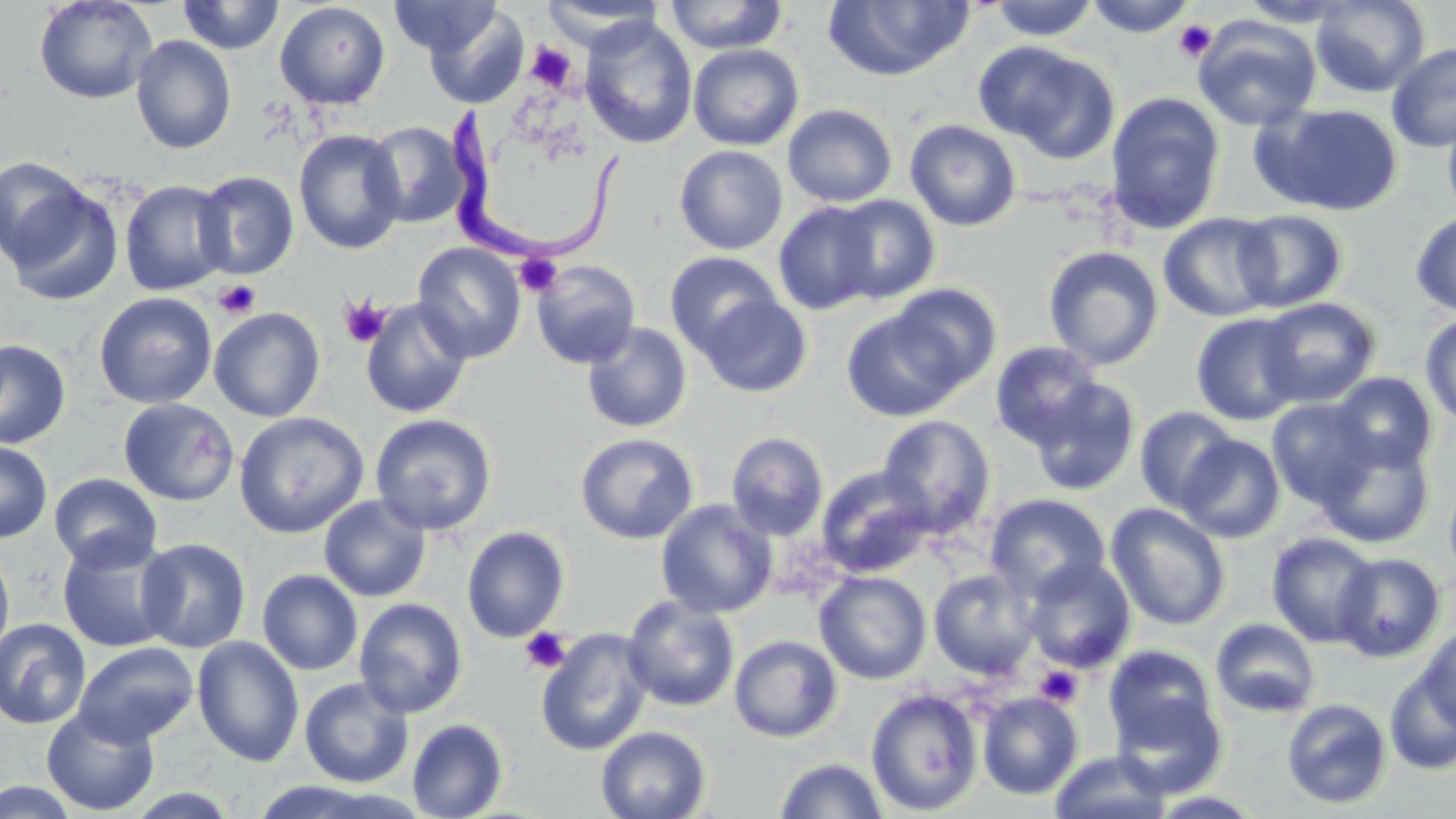

Summary:
  - Coordinate format: approximate bounding boxes as named x1/y1/x2/y2 corners in pixels
  - Uninfected red blood cell locations: (x1=34, y1=0, x2=158, y2=105), (x1=177, y1=0, x2=285, y2=55), (x1=391, y1=0, x2=498, y2=58), (x1=1084, y1=0, x2=1198, y2=38), (x1=1236, y1=0, x2=1357, y2=27), (x1=1310, y1=0, x2=1430, y2=97), (x1=539, y1=1, x2=666, y2=51), (x1=663, y1=1, x2=789, y2=54), (x1=821, y1=1, x2=975, y2=82), (x1=988, y1=1, x2=1099, y2=41), (x1=274, y1=2, x2=391, y2=110), (x1=424, y1=4, x2=528, y2=109), (x1=1192, y1=16, x2=1321, y2=131), (x1=579, y1=17, x2=698, y2=150), (x1=130, y1=35, x2=237, y2=154), (x1=977, y1=42, x2=1119, y2=160), (x1=1386, y1=42, x2=1456, y2=152), (x1=687, y1=43, x2=804, y2=150), (x1=1105, y1=92, x2=1226, y2=235), (x1=783, y1=103, x2=898, y2=208), (x1=1256, y1=103, x2=1404, y2=217), (x1=1441, y1=104, x2=1456, y2=224), (x1=905, y1=119, x2=1022, y2=232), (x1=365, y1=121, x2=468, y2=228), (x1=294, y1=129, x2=406, y2=255), (x1=674, y1=145, x2=788, y2=255), (x1=0, y1=155, x2=93, y2=270), (x1=193, y1=170, x2=299, y2=279), (x1=119, y1=179, x2=233, y2=296), (x1=3, y1=182, x2=124, y2=307), (x1=112, y1=182, x2=223, y2=409), (x1=827, y1=194, x2=941, y2=304), (x1=773, y1=201, x2=883, y2=315), (x1=1233, y1=210, x2=1348, y2=311), (x1=1410, y1=211, x2=1456, y2=316), (x1=1158, y1=212, x2=1281, y2=323), (x1=412, y1=242, x2=526, y2=363), (x1=1043, y1=245, x2=1165, y2=371), (x1=665, y1=251, x2=782, y2=356), (x1=531, y1=260, x2=641, y2=369), (x1=887, y1=284, x2=1001, y2=390), (x1=94, y1=292, x2=217, y2=409), (x1=695, y1=293, x2=813, y2=398), (x1=1257, y1=297, x2=1381, y2=407), (x1=360, y1=299, x2=472, y2=419), (x1=209, y1=307, x2=325, y2=422), (x1=842, y1=308, x2=965, y2=421), (x1=1191, y1=312, x2=1305, y2=426), (x1=1420, y1=312, x2=1456, y2=426), (x1=582, y1=323, x2=692, y2=433), (x1=0, y1=338, x2=71, y2=450), (x1=990, y1=341, x2=1105, y2=451), (x1=1331, y1=372, x2=1437, y2=473), (x1=1026, y1=375, x2=1141, y2=496), (x1=118, y1=398, x2=239, y2=506), (x1=1266, y1=398, x2=1379, y2=510), (x1=1134, y1=406, x2=1240, y2=512), (x1=234, y1=411, x2=368, y2=538), (x1=369, y1=414, x2=497, y2=536), (x1=876, y1=415, x2=995, y2=536), (x1=726, y1=431, x2=829, y2=541), (x1=575, y1=432, x2=698, y2=544), (x1=1314, y1=432, x2=1435, y2=547), (x1=1179, y1=435, x2=1285, y2=542), (x1=0, y1=441, x2=52, y2=542), (x1=815, y1=467, x2=934, y2=578), (x1=1444, y1=472, x2=1456, y2=593), (x1=49, y1=473, x2=163, y2=573), (x1=984, y1=493, x2=1111, y2=601), (x1=319, y1=495, x2=431, y2=603), (x1=656, y1=500, x2=777, y2=619), (x1=1105, y1=503, x2=1231, y2=631), (x1=461, y1=526, x2=569, y2=642), (x1=1266, y1=532, x2=1380, y2=648), (x1=57, y1=536, x2=177, y2=653), (x1=136, y1=537, x2=251, y2=653), (x1=0, y1=544, x2=15, y2=664), (x1=1333, y1=552, x2=1445, y2=662), (x1=1022, y1=558, x2=1136, y2=673), (x1=257, y1=569, x2=363, y2=675), (x1=928, y1=569, x2=1040, y2=679), (x1=813, y1=570, x2=932, y2=685), (x1=621, y1=595, x2=740, y2=712), (x1=353, y1=598, x2=468, y2=719), (x1=0, y1=618, x2=91, y2=729), (x1=1210, y1=618, x2=1321, y2=719), (x1=1416, y1=626, x2=1455, y2=732), (x1=535, y1=627, x2=653, y2=756), (x1=729, y1=634, x2=843, y2=743), (x1=191, y1=636, x2=305, y2=767), (x1=73, y1=642, x2=199, y2=747), (x1=1103, y1=644, x2=1219, y2=755), (x1=1384, y1=669, x2=1456, y2=776), (x1=299, y1=677, x2=414, y2=788), (x1=865, y1=688, x2=983, y2=816), (x1=1109, y1=690, x2=1228, y2=799), (x1=977, y1=691, x2=1084, y2=800), (x1=1281, y1=698, x2=1392, y2=809), (x1=42, y1=706, x2=160, y2=816), (x1=407, y1=718, x2=509, y2=819), (x1=596, y1=726, x2=711, y2=819), (x1=1050, y1=750, x2=1172, y2=819), (x1=775, y1=757, x2=888, y2=818), (x1=0, y1=780, x2=83, y2=818), (x1=1148, y1=791, x2=1269, y2=818)
  - Trypanosoma brucei locations: (x1=432, y1=106, x2=629, y2=266)
  - Platelet locations: (x1=1174, y1=20, x2=1217, y2=62), (x1=525, y1=42, x2=577, y2=92), (x1=514, y1=253, x2=563, y2=297), (x1=213, y1=279, x2=261, y2=319), (x1=338, y1=295, x2=391, y2=347), (x1=520, y1=627, x2=571, y2=674), (x1=1033, y1=665, x2=1084, y2=708)
  - Slide-level diagnosis: Trypanosoma brucei
  - Magnification: 1000x
  - Image size: 1456×819 pixels
  - Stain: May-Grünwald-Giemsa
  - Field of view: one of a larger specimen
  - Preparation: thin blood smear
  - Modality: light microscopy